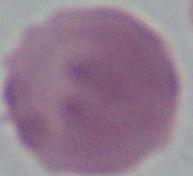

Summary:
  - Magnification: 1000x
  - Identification: red blood cell
  - Modality: micrograph